Classify this cell by malaria status.
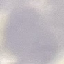
Uninfected.

{
  "stain": "Giemsa",
  "preparation": "thin blood film",
  "capture": "smartphone through the microscope eyepiece",
  "image_type": "cell patch, automatically extracted from a larger field of view and resized to 64 × 64 pixels"
}